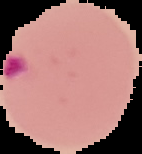

preparation = thin blood smear
image type = cell region segmented out of the field of view; surrounding area masked to black
malaria status = parasitized
image size = 142×154 pixels